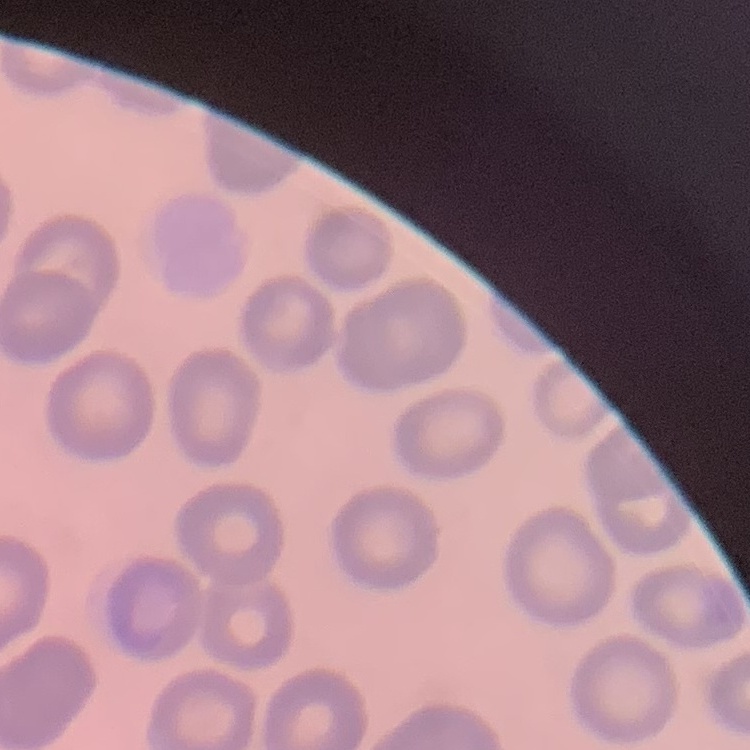

{
  "red_blood_cell_morphology": "no rouleaux formation",
  "preparation": "thin peripheral smear",
  "image_type": "square crop of a larger photomicrograph",
  "stain": "Field's or Giemsa"
}